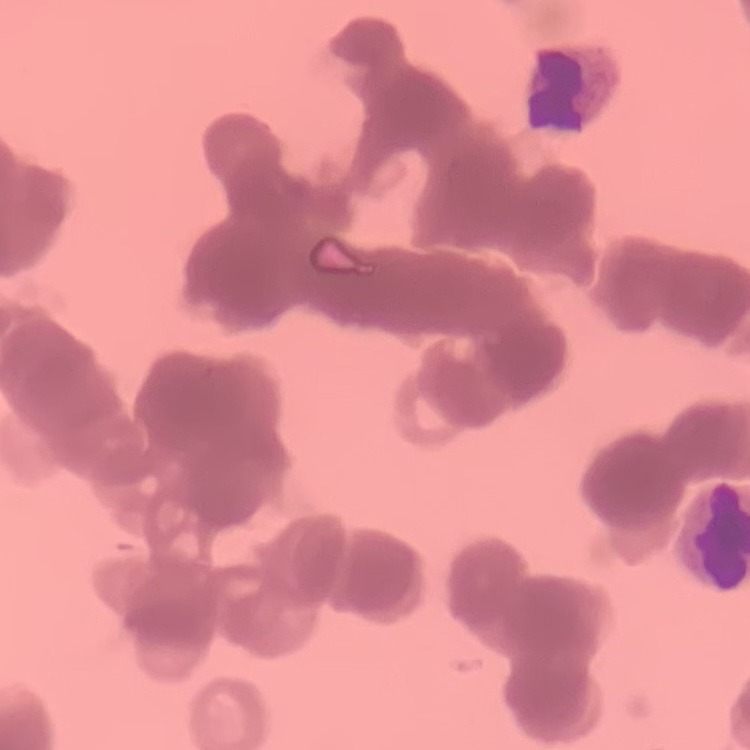
erythrocyte morphology = rouleaux formation
preparation = thin peripheral smear
stain = Field's or Giemsa
image type = one tile cut from a larger photomicrograph